Outline each blood parasite and name the species.
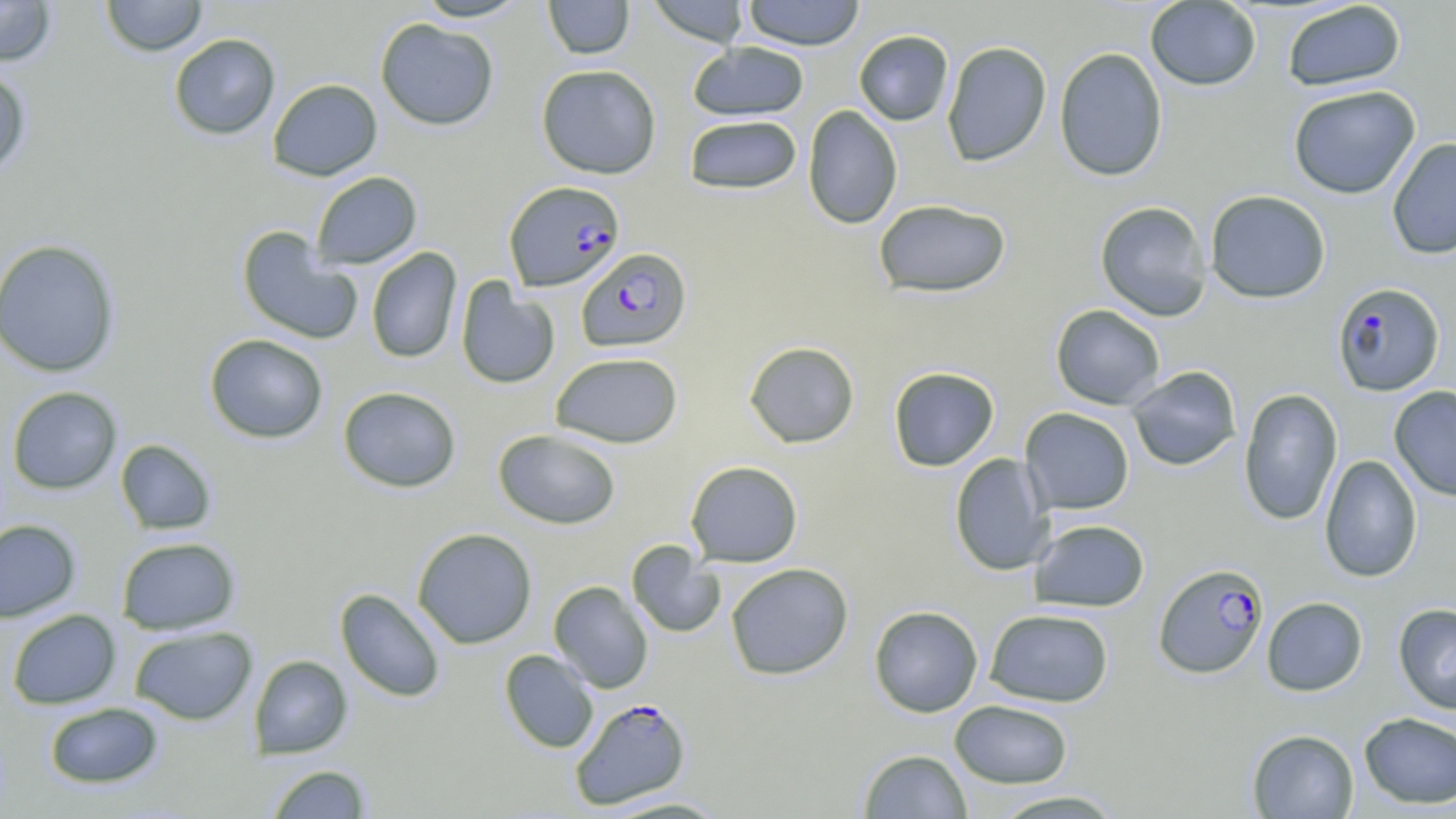
Approximate bounding boxes as [x1, y1, x2, y2] in pixels.
Plasmodium falciparum-infected red blood cells (subset): [504, 180, 625, 292], [576, 247, 692, 352], [1153, 562, 1269, 679], [569, 696, 692, 810].
No Plasmodium ovale, Plasmodium malariae, Plasmodium vivax, Babesia divergens, or Trypanosoma brucei observed.

Summary:
  - Uninfected red blood cell locations (subset): [100, 0, 208, 56], [413, 0, 532, 22], [543, 0, 635, 60], [646, 0, 750, 47], [741, 0, 867, 50], [0, 1, 57, 67], [1145, 1, 1262, 91], [1281, 1, 1407, 92], [375, 18, 499, 131], [854, 30, 954, 126], [168, 33, 281, 140], [941, 41, 1052, 167], [687, 42, 810, 122], [1053, 47, 1168, 182], [536, 64, 662, 179], [0, 66, 31, 178], [267, 78, 382, 181], [1287, 84, 1421, 199], [802, 105, 903, 229], [683, 114, 803, 195], [1386, 137, 1456, 260], [311, 171, 422, 269], [1205, 190, 1331, 304], [873, 199, 1011, 298], [1095, 200, 1212, 321], [236, 226, 363, 345], [0, 239, 122, 377], [366, 247, 462, 364], [456, 278, 560, 390], [1050, 304, 1166, 410], [204, 334, 328, 443], [743, 341, 860, 448], [550, 352, 683, 448], [1126, 365, 1242, 471], [888, 366, 1000, 472], [1389, 385, 1456, 502], [7, 386, 122, 494], [338, 386, 462, 493], [1238, 388, 1343, 526], [1020, 407, 1134, 514], [493, 429, 621, 529], [115, 439, 217, 535], [949, 453, 1053, 576], [1318, 454, 1423, 583], [685, 460, 803, 568], [0, 519, 81, 622], [1029, 519, 1150, 612], [412, 527, 537, 649], [117, 537, 240, 635], [626, 541, 725, 639], [725, 563, 854, 680], [549, 581, 654, 693], [335, 588, 447, 703], [1261, 596, 1368, 696], [1393, 602, 1456, 715], [868, 605, 983, 717], [984, 608, 1114, 707], [6, 609, 121, 710], [129, 625, 258, 725], [499, 650, 599, 753], [249, 654, 352, 759], [949, 699, 1074, 788], [43, 702, 164, 789], [1358, 712, 1456, 809], [1247, 729, 1359, 819], [858, 749, 973, 819], [265, 764, 373, 818], [985, 790, 1129, 818], [599, 795, 733, 817]
  - Slide-level diagnosis: Plasmodium falciparum
  - Magnification: 1000x
  - Image size: 1456×819 pixels
  - Field of view: single
  - Stain: May-Grünwald-Giemsa
  - Preparation: thin blood smear
  - Modality: optical microscopy